State which parasite is depicted.
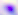
Toxoplasma gondii.

{
  "magnification": "400x",
  "modality": "micrograph"
}